Identify the blood parasite species.
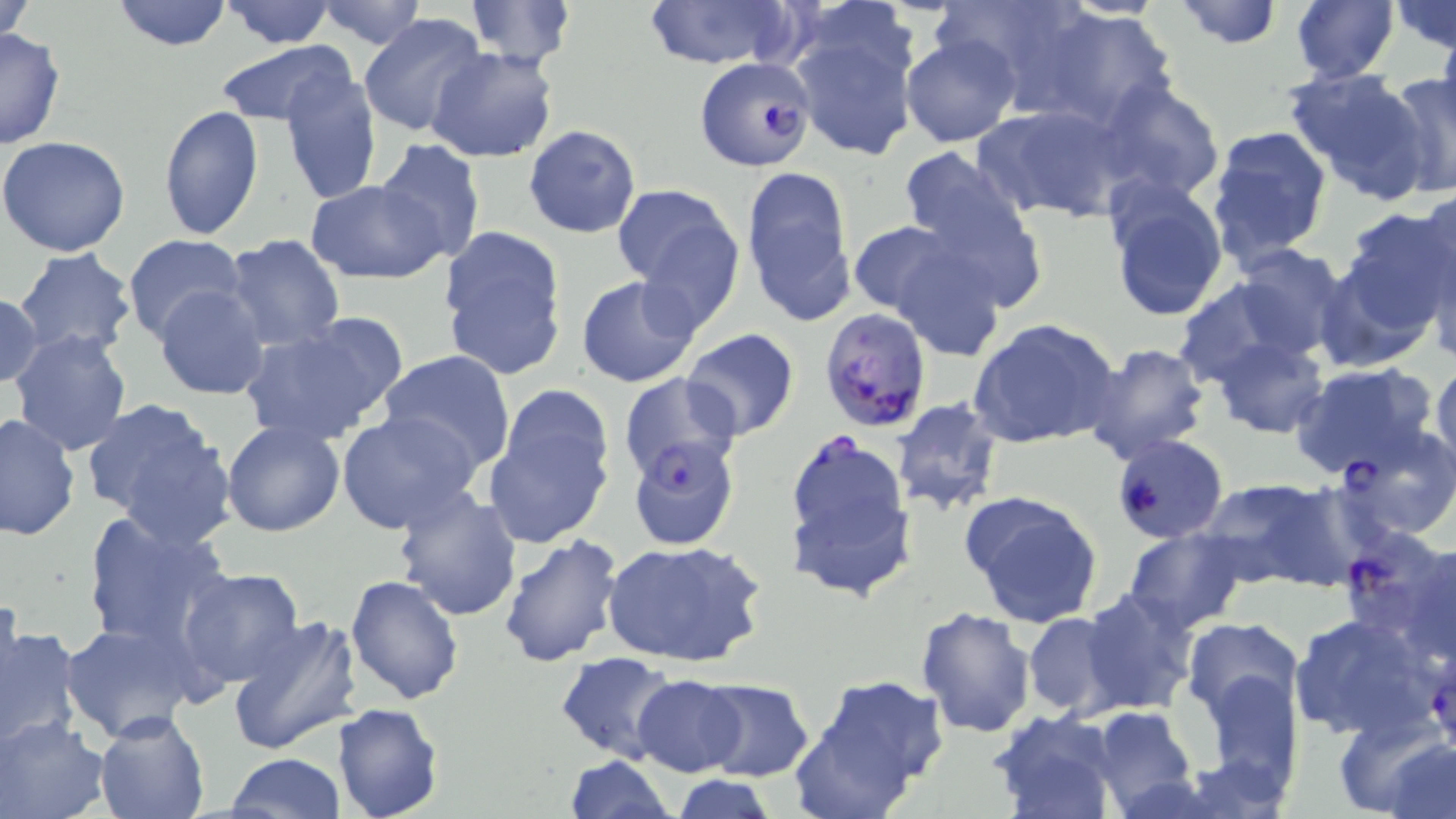

Plasmodium falciparum.

Approximate bounding boxes as [x1, y1, x2, y2] in pixels. Uninfected red blood cell locations: [1, 0, 37, 48], [111, 0, 234, 52], [463, 0, 576, 68], [637, 0, 796, 69], [934, 0, 1094, 102], [1169, 0, 1284, 49], [1289, 0, 1398, 84], [1391, 0, 1455, 52], [219, 1, 338, 48], [313, 1, 430, 51], [1033, 6, 1179, 131], [358, 13, 488, 138], [790, 18, 919, 161], [1436, 20, 1456, 141], [0, 28, 67, 152], [900, 33, 1023, 148], [215, 41, 355, 127], [428, 47, 559, 162], [1283, 67, 1430, 198], [279, 68, 382, 205], [1385, 71, 1455, 199], [1095, 79, 1225, 203], [976, 101, 1131, 224], [158, 105, 264, 239], [524, 125, 641, 238], [1205, 125, 1332, 266], [0, 136, 131, 257], [373, 138, 487, 262], [899, 146, 1041, 291], [742, 167, 857, 323], [1103, 176, 1230, 323], [306, 180, 450, 284], [613, 183, 743, 320], [1412, 187, 1456, 315], [1336, 207, 1452, 347], [847, 220, 963, 318], [438, 227, 570, 379], [125, 235, 248, 343], [223, 235, 346, 352], [887, 242, 1009, 365], [1225, 244, 1355, 363], [12, 247, 140, 361], [575, 274, 701, 388], [1172, 279, 1310, 386], [155, 285, 271, 400], [0, 291, 45, 391], [238, 315, 410, 448], [970, 317, 1122, 451], [680, 328, 800, 442], [9, 329, 133, 457], [1207, 335, 1328, 440], [1083, 342, 1211, 466], [376, 350, 517, 475], [1430, 358, 1456, 477], [1289, 362, 1438, 479], [482, 390, 617, 548], [82, 397, 235, 549], [892, 397, 1005, 519], [336, 410, 483, 536], [0, 412, 79, 541], [222, 419, 345, 537], [781, 428, 917, 550], [626, 441, 741, 556], [1196, 476, 1343, 588], [392, 485, 524, 622], [960, 489, 1104, 628], [792, 500, 916, 609], [79, 510, 230, 654], [1122, 528, 1247, 633], [497, 533, 624, 670], [601, 539, 766, 669], [1406, 541, 1456, 665], [177, 566, 305, 688], [345, 572, 466, 705], [1081, 588, 1199, 716], [916, 606, 1035, 738], [1024, 612, 1125, 718], [1289, 612, 1444, 743], [226, 614, 364, 757], [1181, 616, 1303, 721], [0, 618, 80, 752], [61, 622, 203, 742], [554, 652, 680, 764], [1192, 668, 1305, 805], [792, 674, 948, 817], [632, 676, 747, 776], [696, 679, 815, 782], [330, 704, 444, 819], [1086, 705, 1198, 814], [94, 709, 211, 819], [989, 710, 1122, 819], [1, 716, 110, 819], [1346, 723, 1456, 817], [226, 752, 345, 819], [563, 754, 677, 819], [669, 773, 783, 819]. Plasmodium falciparum-infected red blood cell locations: [694, 55, 814, 170], [820, 305, 933, 431], [619, 373, 741, 495], [1335, 426, 1456, 541], [1112, 434, 1228, 544], [1336, 526, 1455, 644]. May-Grünwald-Giemsa stain. Image is 1456×819 pixels. Optical microscopy. Thin blood smear. One field of a larger specimen. Captured at 1000x magnification.